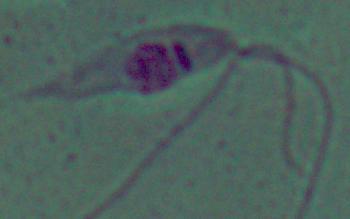
Summary:
  - Modality: micrograph
  - Magnification: 1000x
  - Identification: Leishmania